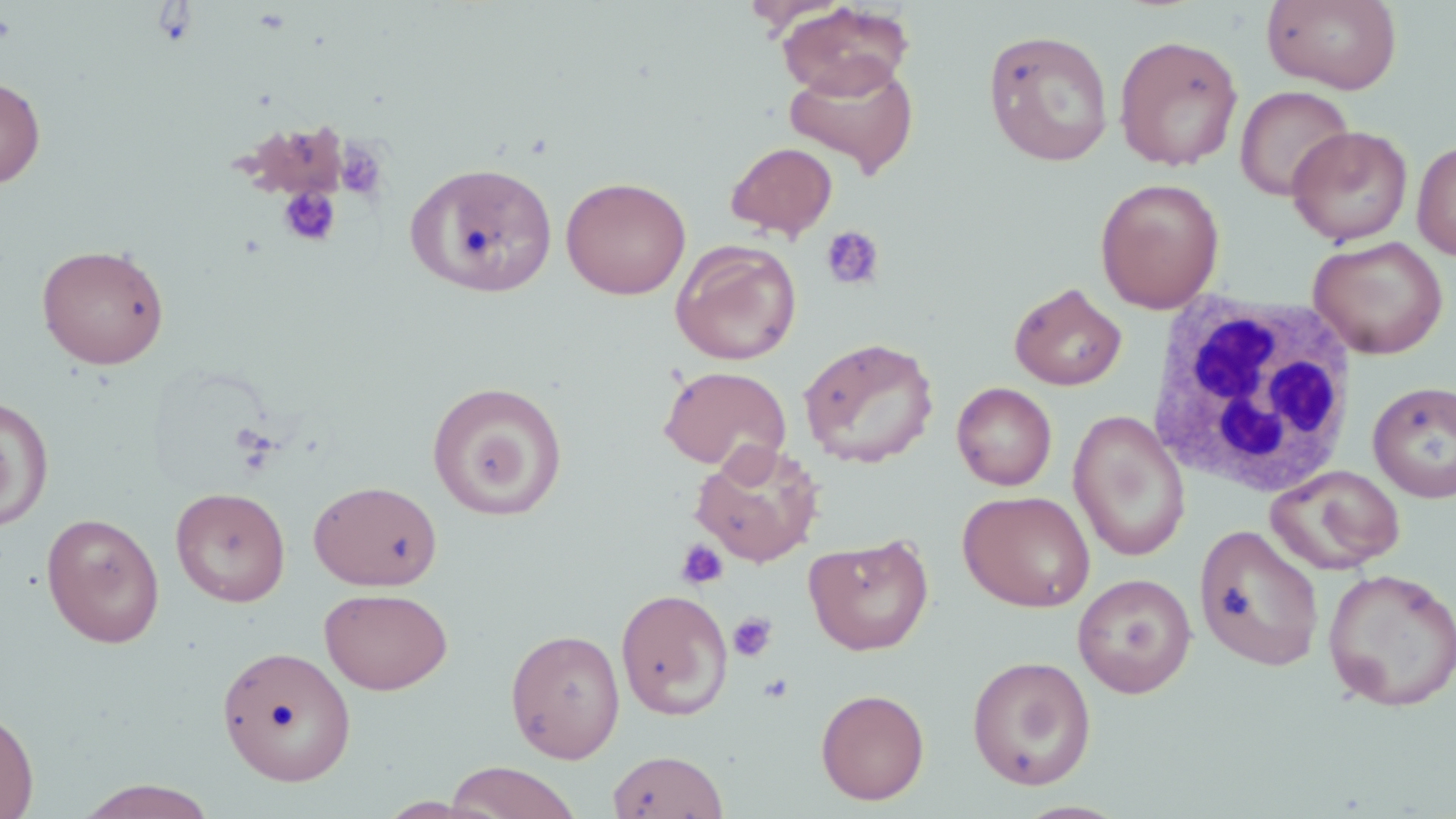

Summary:
  - Coordinate format: approximate bounding boxes as (x1,y1)-(x2,y2) corner pairs in pixels
  - Uninfected red blood cell locations: (1262,0)-(1402,94), (777,2)-(915,99), (983,28)-(1115,167), (1113,34)-(1244,171), (783,58)-(918,177), (0,76)-(46,188), (1234,85)-(1355,201), (1287,125)-(1414,246), (1412,139)-(1456,260), (725,141)-(839,241), (408,162)-(559,298), (561,175)-(691,300), (1094,176)-(1225,313), (1309,235)-(1448,359), (671,239)-(802,365), (36,242)-(170,369), (1009,283)-(1127,391), (798,337)-(939,469), (658,365)-(791,472), (1367,380)-(1456,502), (427,381)-(567,520), (951,382)-(1057,491), (0,396)-(55,531), (1068,410)-(1191,562), (690,441)-(825,567), (1266,465)-(1406,575), (309,479)-(444,591), (170,486)-(291,607), (958,490)-(1095,612), (41,512)-(165,648), (1194,523)-(1324,672), (803,533)-(935,655), (1322,567)-(1456,712), (1072,573)-(1197,698), (319,587)-(453,694), (615,588)-(733,721), (505,627)-(626,763), (217,645)-(356,786), (967,655)-(1097,790), (815,688)-(930,805), (0,704)-(38,819), (607,749)-(729,819), (443,762)-(582,819), (71,780)-(222,818)
  - Platelet locations: (334,139)-(389,203), (277,185)-(341,248), (820,225)-(885,292), (675,539)-(728,591), (728,611)-(778,663), (758,673)-(794,703)
  - White blood cell locations: (1143,294)-(1360,500)
  - Slide-level diagnosis: negative for blood parasites
  - Stain: May-Grünwald-Giemsa
  - Image size: 1456×819 pixels
  - Field of view: one of a larger specimen
  - Magnification: 1000x
  - Modality: light microscopy
  - Preparation: thin blood film